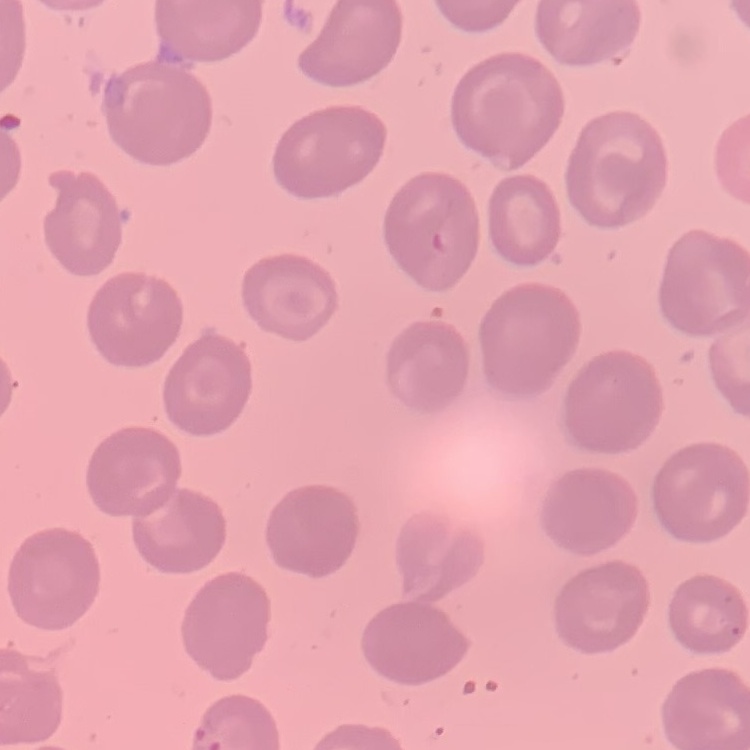

red blood cell morphology = no rouleaux formation
stain = Field's or Giemsa
image type = one tile cut from a larger photomicrograph
preparation = thin blood smear